Evaluate for Plasmodium parasites.
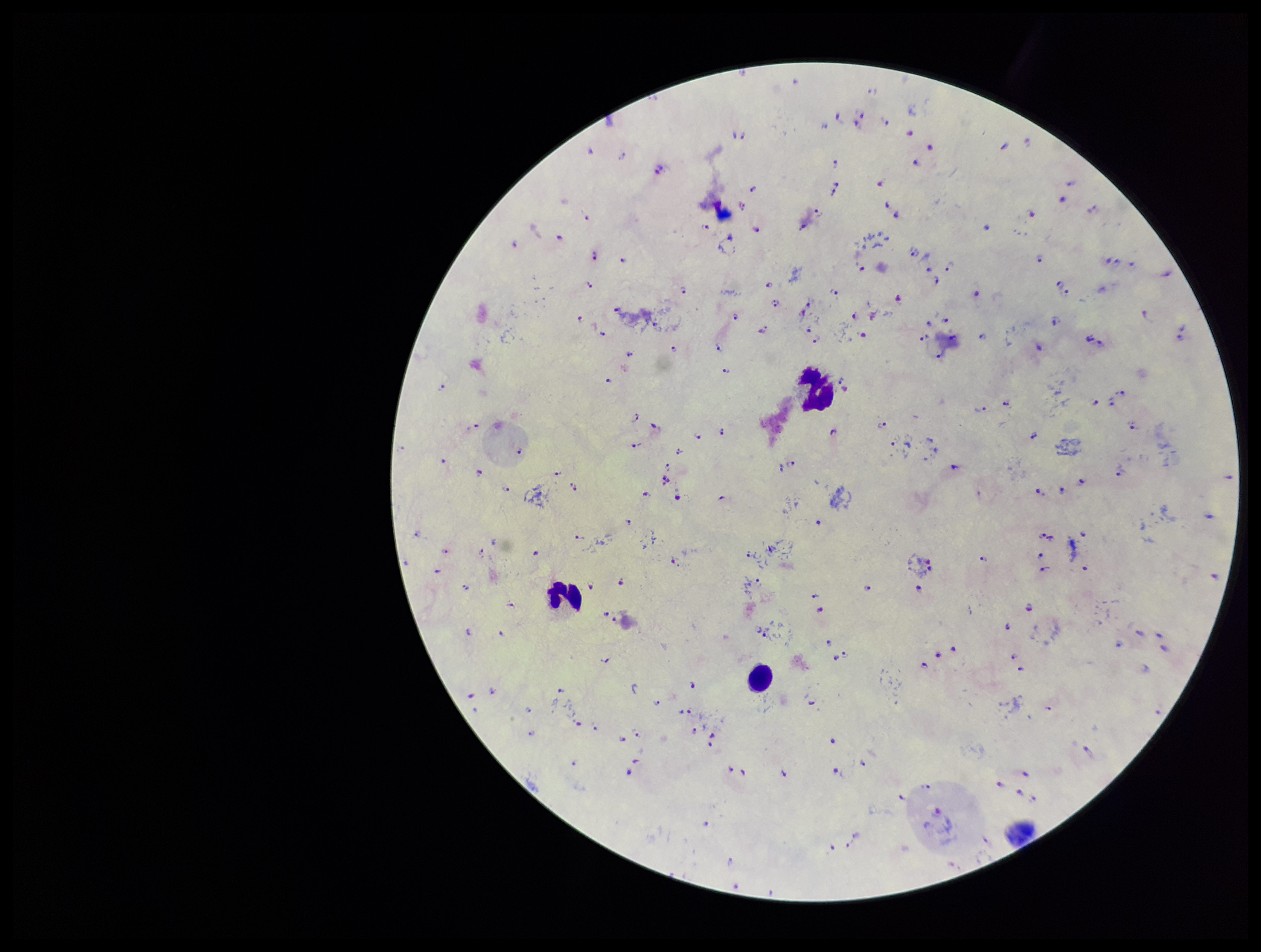
Seen.

Summary:
  - Field of view: single
  - Stain: Giemsa
  - Image size: 1261×952 pixels
  - Species reported for this patient: Plasmodium falciparum
  - Capture: smartphone photograph through the microscope eyepiece
  - Patient malaria status: positive
  - Leukocyte count: 3
  - Parasite count: 121
  - Preparation: thick smear